Assess the morphology of the red blood cells.
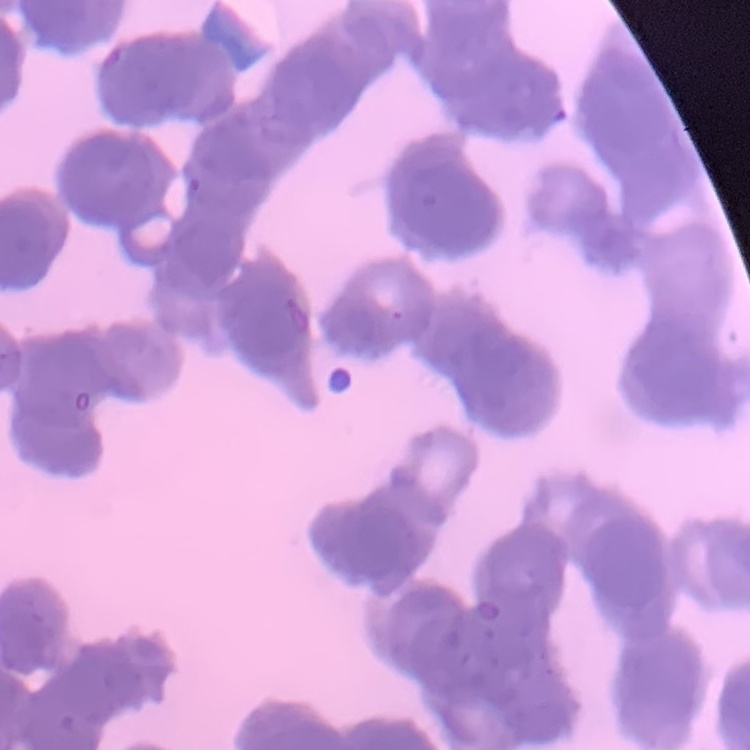

Rouleaux formation.

stain: Field's or Giemsa
image_type: one tile cut from a larger photomicrograph
preparation: thin peripheral smear